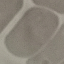
{
  "result": "no malaria parasites seen",
  "capture": "smartphone through the microscope eyepiece",
  "stain": "Giemsa",
  "image_type": "automatically extracted cell patch, resized to 64 × 64 pixels",
  "preparation": "thin blood film"
}